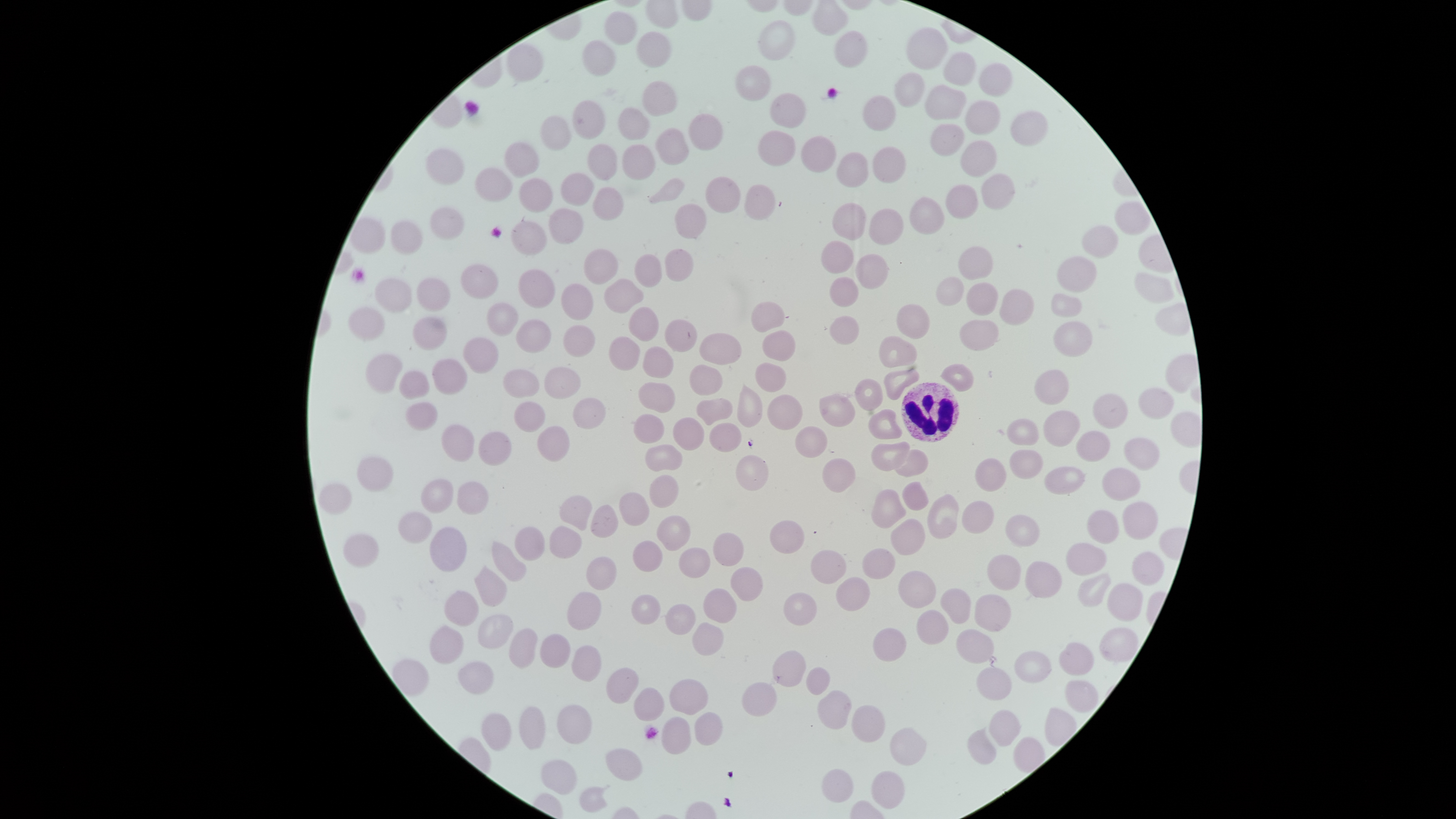

Approximate bounding boxes as {left, top, right, bottom} in pixels.
Summary:
  - White blood cells: {901, 383, 959, 441}
  - Uninfected red blood cells: {605, 11, 639, 45}, {757, 20, 795, 61}, {906, 27, 948, 70}, {833, 30, 869, 69}, {637, 32, 673, 70}, {584, 39, 618, 77}, {505, 43, 543, 82}, {942, 52, 977, 86}, {980, 62, 1014, 99}, {735, 65, 771, 103}, {895, 72, 925, 109}, {643, 80, 678, 116}, {926, 84, 967, 121}, {770, 91, 807, 131}, {864, 96, 897, 131}, {964, 99, 1002, 136}, {572, 101, 606, 138}, {618, 106, 651, 140}, {1011, 109, 1047, 146}, {689, 114, 725, 151}, {542, 115, 573, 150}, {932, 123, 965, 156}, {654, 127, 689, 165}, {759, 130, 795, 167}, {800, 136, 836, 172}, {961, 139, 997, 177}, {504, 141, 542, 177}, {585, 141, 619, 179}, {623, 144, 657, 180}, {874, 146, 907, 184}, {427, 148, 465, 185}, {837, 151, 869, 186}, {475, 168, 512, 203}, {561, 173, 594, 209}, {980, 173, 1017, 209}, {705, 177, 741, 213}, {519, 178, 554, 213}, {648, 178, 685, 203}, {946, 184, 979, 219}, {744, 185, 776, 220}, {594, 186, 625, 220}, {908, 197, 945, 235}, {832, 201, 867, 241}, {1116, 201, 1151, 235}, {674, 204, 707, 240}, {432, 207, 465, 240}, {549, 208, 584, 244}, {868, 208, 903, 246}, {391, 220, 423, 254}, {511, 220, 548, 255}, {1082, 224, 1117, 257}, {820, 241, 855, 273}, {958, 247, 994, 280}, {584, 249, 617, 285}, {665, 250, 693, 282}, {634, 253, 662, 290}, {856, 255, 889, 290}, {1056, 257, 1098, 294}, {459, 264, 498, 299}, {518, 269, 555, 308}, {1135, 272, 1175, 303}, {830, 276, 860, 306}, {937, 276, 964, 306}, {375, 278, 413, 313}, {417, 279, 451, 311}, {605, 279, 644, 315}, {966, 281, 998, 316}, {562, 283, 593, 321}, {998, 288, 1035, 325}, {1051, 293, 1083, 318}, {488, 301, 519, 336}, {753, 302, 786, 332}, {897, 304, 931, 340}, {349, 306, 385, 341}, {628, 307, 658, 342}, {412, 316, 447, 350}, {828, 316, 861, 346}, {665, 317, 698, 353}, {960, 318, 1000, 351}, {515, 319, 553, 352}, {1052, 321, 1093, 358}, {564, 324, 597, 356}, {762, 330, 797, 362}, {699, 333, 743, 365}, {880, 335, 917, 367}, {462, 337, 498, 374}, {642, 346, 674, 381}, {365, 354, 402, 394}, {431, 359, 467, 395}, {690, 363, 722, 395}, {754, 363, 788, 394}, {939, 363, 976, 392}, {543, 366, 580, 400}, {883, 368, 919, 402}, {504, 369, 538, 400}, {399, 370, 430, 399}, {1033, 370, 1069, 406}, {855, 377, 883, 412}, {638, 382, 674, 414}, {736, 383, 763, 428}, {1139, 387, 1175, 418}, {819, 392, 857, 426}, {1092, 394, 1129, 428}, {767, 395, 803, 430}, {573, 398, 607, 431}, {697, 398, 733, 427}, {406, 401, 437, 431}, {516, 401, 545, 432}, {868, 408, 902, 440}, {1041, 410, 1079, 449}, {633, 413, 667, 443}, {672, 417, 704, 452}, {1006, 417, 1040, 446}, {709, 423, 743, 452}, {442, 424, 475, 462}, {536, 426, 570, 461}, {795, 426, 828, 457}, {1076, 430, 1111, 463}, {477, 432, 511, 465}, {1124, 438, 1159, 470}, {871, 441, 911, 471}, {645, 444, 682, 473}, {892, 449, 928, 476}, {1009, 449, 1043, 479}, {736, 454, 770, 491}, {355, 455, 395, 492}, {822, 458, 857, 493}, {975, 458, 1007, 492}, {1043, 466, 1086, 495}, {1101, 469, 1141, 501}, {649, 474, 679, 508}, {421, 479, 456, 512}, {319, 482, 352, 513}, {457, 482, 489, 515}, {903, 482, 928, 511}, {871, 488, 908, 529}, {619, 493, 650, 525}, {927, 494, 960, 538}, {559, 495, 593, 532}, {961, 499, 995, 534}, {1123, 501, 1159, 540}, {591, 504, 618, 539}, {1086, 510, 1120, 544}, {399, 511, 433, 542}, {1006, 514, 1040, 547}, {656, 515, 692, 550}, {890, 517, 926, 557}, {770, 520, 806, 554}, {430, 526, 467, 572}, {515, 527, 543, 560}, {550, 527, 583, 558}, {343, 532, 379, 567}, {713, 532, 745, 566}, {491, 539, 526, 582}, {633, 540, 662, 573}, {1065, 543, 1107, 576}, {680, 548, 710, 579}, {861, 548, 895, 580}, {811, 549, 848, 585}, {1132, 552, 1164, 586}, {986, 555, 1021, 591}, {587, 557, 617, 590}, {1023, 560, 1062, 598}, {473, 565, 508, 606}, {731, 567, 763, 602}, {899, 570, 937, 608}, {1078, 573, 1112, 607}, {834, 577, 870, 612}, {1108, 582, 1143, 621}, {941, 587, 971, 624}, {703, 588, 737, 623}, {445, 590, 479, 626}, {567, 591, 602, 631}, {784, 593, 817, 626}, {975, 593, 1011, 633}, {632, 596, 660, 625}, {665, 604, 695, 635}, {915, 608, 948, 645}, {478, 614, 514, 649}, {692, 622, 724, 656}, {429, 625, 464, 664}, {1098, 627, 1139, 662}, {509, 628, 538, 667}, {955, 628, 995, 662}, {872, 629, 907, 662}, {540, 633, 570, 668}, {1058, 642, 1094, 676}, {573, 644, 601, 681}, {772, 651, 807, 687}, {1014, 651, 1053, 683}, {459, 660, 494, 694}, {975, 667, 1012, 700}, {606, 668, 639, 705}, {806, 669, 831, 694}, {669, 679, 707, 716}, {1064, 679, 1099, 713}, {742, 682, 777, 717}, {634, 687, 666, 722}, {817, 690, 851, 729}, {852, 704, 884, 742}, {557, 705, 593, 744}, {519, 706, 547, 749}, {989, 710, 1020, 747}, {695, 712, 722, 744}, {480, 713, 514, 751}, {661, 717, 692, 754}, {890, 727, 927, 767}, {966, 728, 997, 764}, {605, 747, 643, 781}, {541, 760, 577, 795}, {822, 769, 853, 804}, {870, 770, 905, 809}
  - Stain: Giemsa
  - Visible region: circular
  - Capture: smartphone photograph through the microscope eyepiece
  - Image size: 1456×819 pixels
  - Presence: no malaria parasites detected
  - Preparation: thin smear of blood
  - Field of view: single